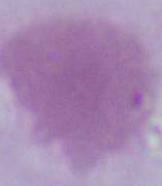

magnification = 1000x
modality = photomicrograph
identification = erythrocyte